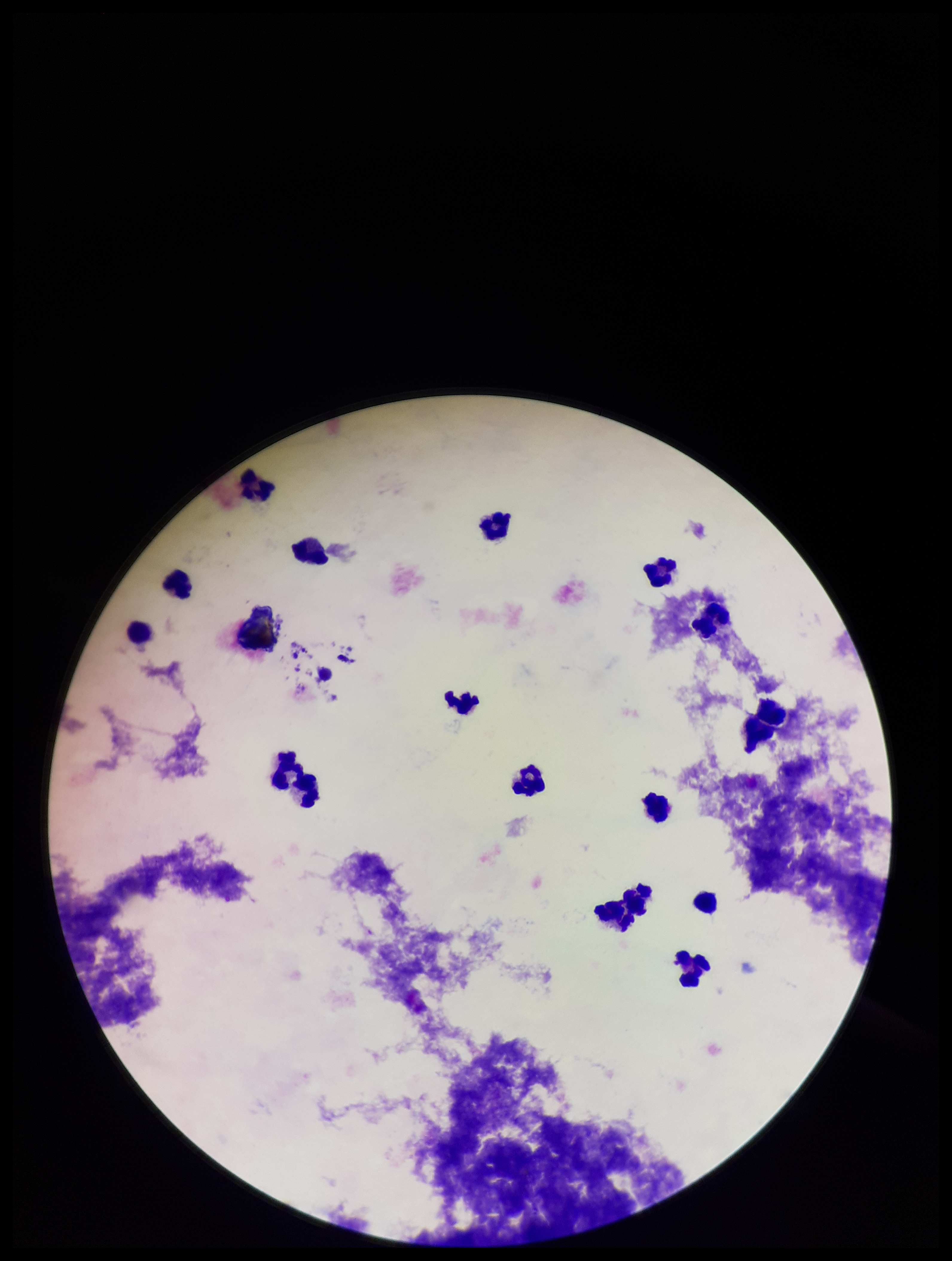
patient malaria status = negative
field of view = one from this slide
stain = Giemsa
Plasmodium parasites = none seen
parasite count = 0
preparation = thick blood smear
leukocyte count = 15
capture = smartphone photograph through the microscope eyepiece
image size = 952×1261 pixels